Locate leukocytes (white blood cells).
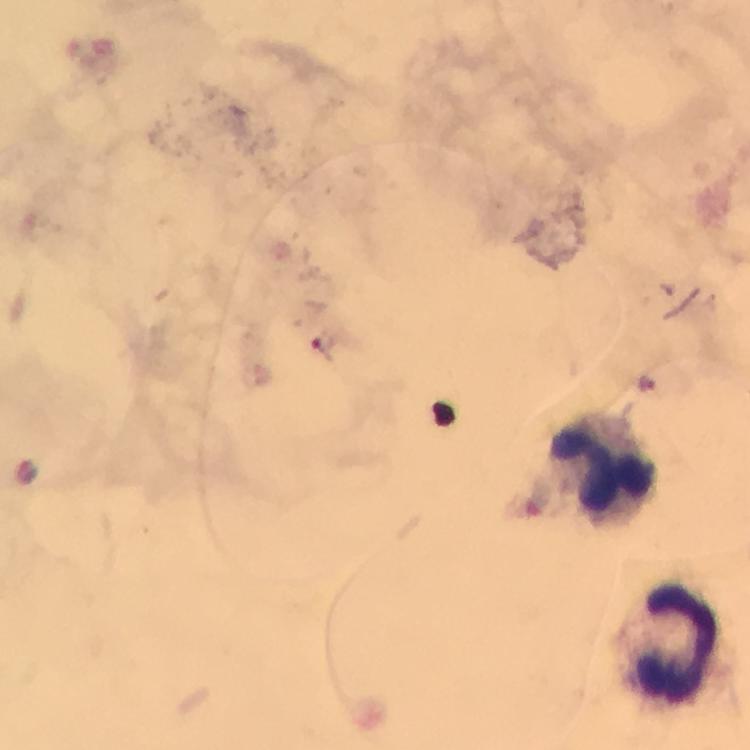
Approximate object centers, in pixels from the top-left corner.
Leukocytes: (x=606, y=470), (x=679, y=645).

Plasmodium parasite locations: (x=647, y=385). 100x magnification. Image is 750×750 pixels. Photographed through the microscope with a smartphone camera. From a malaria diagnostic workup. Giemsa stain. Immersion oil applied. Cropped region of a single field of view. Thick blood film.